Report the malaria status of this cell.
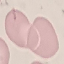

Uninfected.

Summary:
  - Preparation: thin smear
  - Image type: automatically extracted cell patch, resized to 64 × 64 pixels
  - Capture: smartphone camera at the microscope eyepiece
  - Stain: Giemsa